Locate platelets.
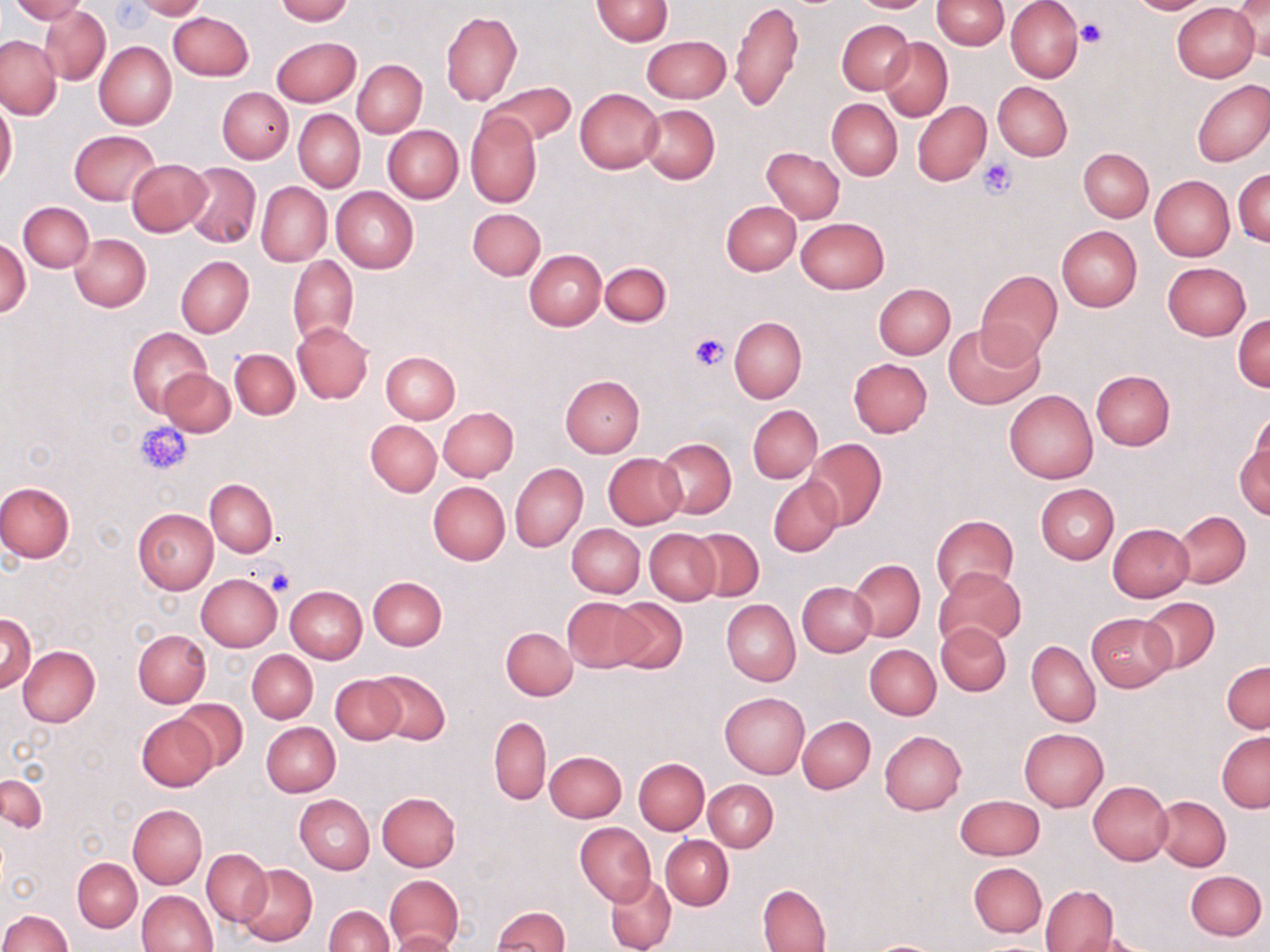
Approximate bounding boxes as named x1/y1/x2/y2 corners in pixels.
Platelets: (x1=1077, y1=19, x2=1105, y2=48), (x1=977, y1=156, x2=1017, y2=199), (x1=689, y1=334, x2=730, y2=371), (x1=136, y1=422, x2=192, y2=475), (x1=264, y1=568, x2=295, y2=596).

Uninfected red blood cell locations: (x1=10, y1=0, x2=87, y2=23), (x1=131, y1=0, x2=206, y2=19), (x1=276, y1=0, x2=352, y2=24), (x1=592, y1=0, x2=672, y2=45), (x1=730, y1=0, x2=802, y2=112), (x1=848, y1=0, x2=936, y2=13), (x1=932, y1=0, x2=1009, y2=50), (x1=1006, y1=0, x2=1082, y2=82), (x1=1127, y1=0, x2=1212, y2=15), (x1=1229, y1=0, x2=1269, y2=64), (x1=1172, y1=3, x2=1259, y2=81), (x1=41, y1=5, x2=110, y2=84), (x1=169, y1=11, x2=253, y2=80), (x1=440, y1=12, x2=522, y2=106), (x1=837, y1=19, x2=915, y2=95), (x1=1, y1=35, x2=61, y2=119), (x1=643, y1=35, x2=729, y2=102), (x1=271, y1=37, x2=360, y2=107), (x1=880, y1=37, x2=953, y2=121), (x1=94, y1=41, x2=176, y2=129), (x1=353, y1=59, x2=426, y2=138), (x1=1192, y1=79, x2=1270, y2=166), (x1=482, y1=81, x2=575, y2=147), (x1=993, y1=82, x2=1072, y2=161), (x1=219, y1=88, x2=292, y2=162), (x1=575, y1=88, x2=664, y2=173), (x1=827, y1=98, x2=902, y2=180), (x1=0, y1=100, x2=17, y2=188), (x1=913, y1=101, x2=991, y2=187), (x1=639, y1=105, x2=719, y2=184), (x1=294, y1=109, x2=364, y2=192), (x1=466, y1=111, x2=542, y2=208), (x1=383, y1=124, x2=463, y2=203), (x1=69, y1=130, x2=160, y2=204), (x1=761, y1=147, x2=845, y2=222), (x1=1078, y1=147, x2=1154, y2=222), (x1=126, y1=158, x2=211, y2=236), (x1=182, y1=162, x2=260, y2=247), (x1=1234, y1=170, x2=1270, y2=246), (x1=1150, y1=175, x2=1235, y2=261), (x1=256, y1=182, x2=331, y2=267), (x1=331, y1=187, x2=419, y2=273), (x1=721, y1=200, x2=801, y2=275), (x1=18, y1=201, x2=93, y2=273), (x1=467, y1=208, x2=545, y2=280), (x1=795, y1=216, x2=889, y2=293), (x1=1057, y1=225, x2=1142, y2=311), (x1=69, y1=234, x2=150, y2=311), (x1=0, y1=236, x2=31, y2=319), (x1=525, y1=249, x2=607, y2=330), (x1=176, y1=255, x2=254, y2=337), (x1=288, y1=255, x2=358, y2=345), (x1=600, y1=261, x2=670, y2=326), (x1=1163, y1=262, x2=1251, y2=340), (x1=976, y1=271, x2=1063, y2=359), (x1=873, y1=283, x2=955, y2=359), (x1=1233, y1=314, x2=1270, y2=392), (x1=729, y1=316, x2=806, y2=403), (x1=292, y1=322, x2=373, y2=404), (x1=943, y1=322, x2=1045, y2=409), (x1=128, y1=327, x2=212, y2=418), (x1=229, y1=348, x2=300, y2=419), (x1=381, y1=350, x2=461, y2=424), (x1=848, y1=358, x2=932, y2=437), (x1=158, y1=368, x2=235, y2=438), (x1=1090, y1=369, x2=1175, y2=449), (x1=559, y1=375, x2=645, y2=458), (x1=1004, y1=390, x2=1098, y2=483), (x1=749, y1=404, x2=822, y2=483), (x1=438, y1=407, x2=518, y2=480), (x1=1246, y1=410, x2=1270, y2=490), (x1=366, y1=420, x2=441, y2=496), (x1=1236, y1=435, x2=1269, y2=522), (x1=804, y1=439, x2=887, y2=528), (x1=655, y1=440, x2=735, y2=518), (x1=603, y1=452, x2=686, y2=529), (x1=510, y1=464, x2=586, y2=551), (x1=769, y1=478, x2=842, y2=557), (x1=205, y1=479, x2=278, y2=557), (x1=0, y1=481, x2=75, y2=562), (x1=428, y1=481, x2=510, y2=566), (x1=1035, y1=484, x2=1119, y2=564), (x1=133, y1=508, x2=219, y2=595), (x1=1172, y1=511, x2=1251, y2=588), (x1=930, y1=515, x2=1018, y2=599), (x1=1106, y1=523, x2=1194, y2=602), (x1=567, y1=524, x2=645, y2=598), (x1=645, y1=528, x2=720, y2=604), (x1=689, y1=528, x2=764, y2=601), (x1=849, y1=559, x2=924, y2=642), (x1=933, y1=567, x2=1027, y2=649), (x1=196, y1=574, x2=282, y2=652), (x1=369, y1=576, x2=447, y2=651), (x1=797, y1=582, x2=876, y2=657), (x1=285, y1=586, x2=367, y2=663), (x1=608, y1=596, x2=688, y2=673), (x1=563, y1=597, x2=648, y2=672), (x1=1140, y1=597, x2=1219, y2=672), (x1=721, y1=599, x2=800, y2=686), (x1=0, y1=613, x2=36, y2=693), (x1=1086, y1=613, x2=1175, y2=691), (x1=936, y1=622, x2=1011, y2=696), (x1=500, y1=627, x2=577, y2=700), (x1=133, y1=630, x2=210, y2=707), (x1=1027, y1=640, x2=1099, y2=726), (x1=865, y1=644, x2=940, y2=720), (x1=18, y1=647, x2=99, y2=727), (x1=247, y1=651, x2=317, y2=722), (x1=1222, y1=661, x2=1269, y2=734), (x1=369, y1=669, x2=451, y2=745), (x1=330, y1=674, x2=406, y2=745), (x1=720, y1=692, x2=809, y2=777), (x1=175, y1=698, x2=246, y2=770), (x1=137, y1=715, x2=218, y2=791), (x1=489, y1=717, x2=551, y2=804), (x1=797, y1=717, x2=875, y2=793), (x1=261, y1=721, x2=340, y2=796), (x1=1018, y1=727, x2=1109, y2=811), (x1=880, y1=730, x2=967, y2=815), (x1=1217, y1=730, x2=1270, y2=812), (x1=544, y1=750, x2=627, y2=823), (x1=634, y1=758, x2=709, y2=835), (x1=1, y1=776, x2=47, y2=833), (x1=704, y1=779, x2=778, y2=851), (x1=1089, y1=781, x2=1173, y2=865), (x1=377, y1=791, x2=461, y2=870), (x1=955, y1=794, x2=1044, y2=860), (x1=295, y1=795, x2=375, y2=874), (x1=1153, y1=795, x2=1230, y2=870), (x1=128, y1=805, x2=207, y2=888), (x1=576, y1=822, x2=655, y2=906), (x1=661, y1=835, x2=733, y2=909), (x1=201, y1=849, x2=271, y2=927), (x1=72, y1=858, x2=141, y2=931), (x1=968, y1=862, x2=1046, y2=937), (x1=237, y1=863, x2=318, y2=946), (x1=1185, y1=870, x2=1266, y2=940), (x1=385, y1=874, x2=464, y2=948), (x1=606, y1=874, x2=676, y2=952), (x1=758, y1=884, x2=831, y2=951), (x1=1040, y1=885, x2=1119, y2=951), (x1=138, y1=890, x2=217, y2=952), (x1=323, y1=905, x2=393, y2=952), (x1=492, y1=906, x2=570, y2=951), (x1=0, y1=909, x2=72, y2=952), (x1=389, y1=930, x2=456, y2=952), (x1=1066, y1=931, x2=1150, y2=952), (x1=860, y1=939, x2=952, y2=952). Slide-level diagnosis: negative for blood parasites. Light microscopy. May-Grünwald-Giemsa-stained preparation. Thin blood smear. Image is 1270×952 pixels. Captured at 1000x magnification. Single field of view.